Locate and identify every blood parasite.
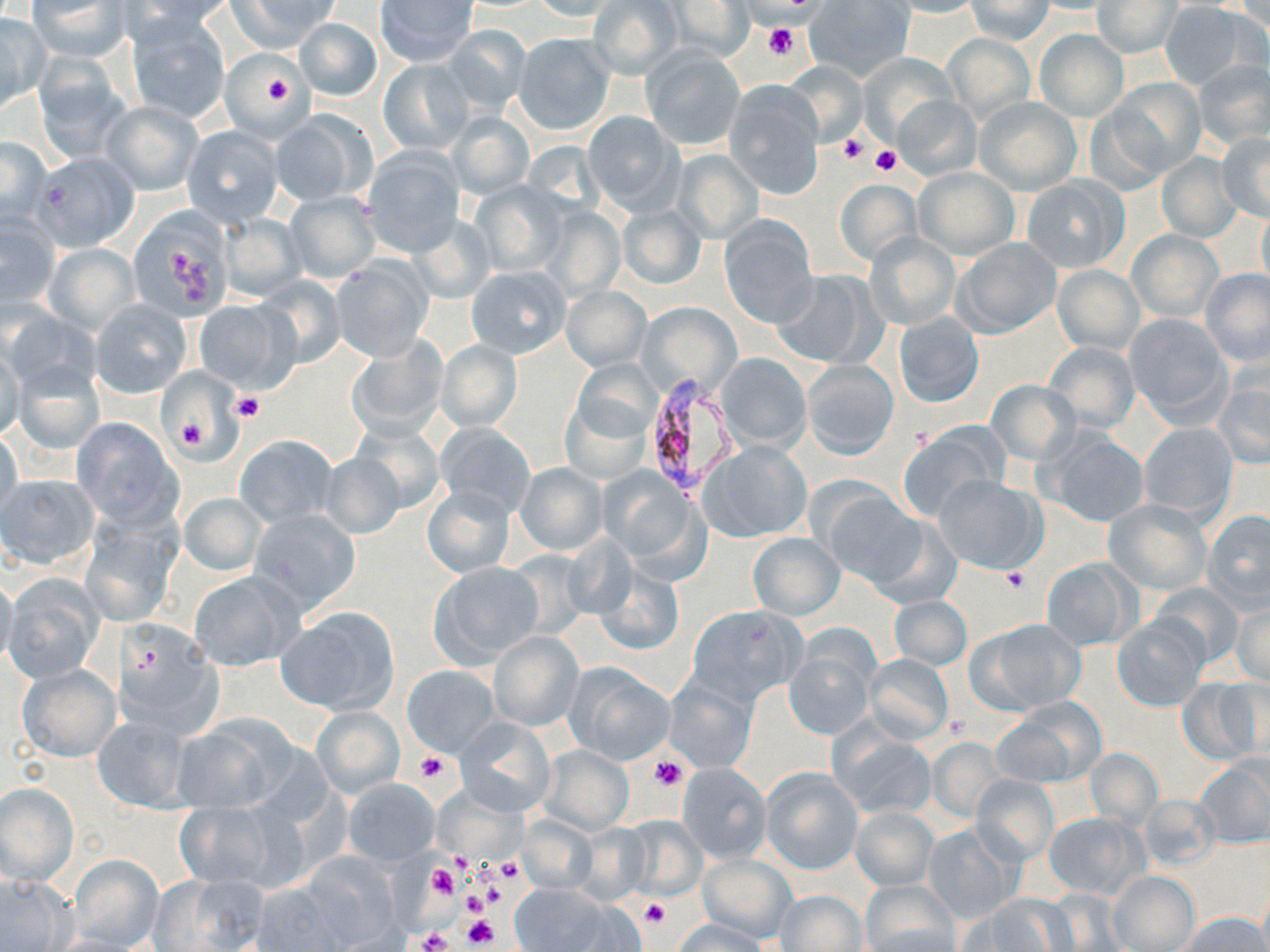
Approximate bounding boxes as (x1, y1, x2, y2) in pixels.
Plasmodium falciparum-infected red blood cells: (640, 375, 740, 498).
No Plasmodium ovale, Plasmodium malariae, Plasmodium vivax, Babesia divergens, or Trypanosoma brucei observed.

slide-level diagnosis = Plasmodium falciparum
preparation = thin blood film
platelet locations = approximate bounding boxes as (x1, y1, x2, y2) in pixels: (764, 24, 798, 58), (253, 66, 298, 112), (838, 131, 870, 163), (843, 138, 888, 170), (869, 147, 901, 176), (233, 393, 265, 421), (170, 408, 218, 458), (1002, 568, 1031, 592), (415, 751, 451, 784), (648, 755, 689, 792), (452, 852, 473, 877), (495, 857, 526, 884), (427, 864, 458, 899), (478, 879, 509, 909), (457, 890, 489, 919), (639, 899, 670, 929), (463, 914, 499, 948), (415, 927, 453, 952)
modality = light microscopy
image size = 1270×952 pixels
uninfected red blood cell locations = approximate bounding boxes as (x1, y1, x2, y2) in pixels: (27, 0, 131, 62), (124, 0, 236, 35), (376, 0, 479, 66), (659, 0, 759, 63), (803, 0, 916, 82), (882, 0, 984, 18), (228, 1, 337, 52), (526, 1, 625, 22), (588, 1, 684, 79), (964, 1, 1056, 43), (1094, 1, 1182, 58), (1158, 4, 1256, 89), (0, 13, 47, 111), (123, 14, 232, 124), (293, 17, 383, 101), (439, 24, 533, 115), (1034, 29, 1129, 122), (511, 33, 615, 135), (942, 34, 1035, 125), (639, 46, 747, 151), (221, 52, 309, 135), (856, 54, 959, 146), (378, 58, 472, 155), (1194, 59, 1270, 150), (33, 60, 131, 163), (781, 60, 867, 148), (1106, 78, 1207, 176), (722, 81, 826, 198), (893, 95, 983, 181), (973, 97, 1081, 195), (101, 101, 202, 195), (269, 111, 378, 207), (447, 111, 535, 199), (582, 111, 686, 216), (181, 126, 283, 226), (1215, 131, 1270, 224), (0, 135, 51, 229), (361, 149, 466, 257), (671, 149, 764, 243), (31, 151, 139, 251), (1155, 152, 1242, 243), (914, 166, 1019, 259), (1019, 175, 1128, 273), (832, 180, 924, 266), (470, 181, 572, 277), (284, 190, 381, 284), (1256, 203, 1270, 300), (614, 204, 707, 291), (539, 206, 625, 301), (124, 207, 234, 319), (218, 213, 305, 301), (407, 214, 497, 303), (718, 215, 819, 328), (1, 216, 62, 311), (1127, 229, 1225, 324), (864, 233, 960, 331), (952, 238, 1062, 339), (43, 243, 139, 334), (329, 255, 435, 361), (1052, 264, 1144, 354), (466, 265, 571, 359), (1200, 268, 1270, 368), (771, 269, 885, 371), (251, 275, 348, 368), (561, 286, 652, 371), (90, 300, 191, 397), (192, 300, 300, 393), (634, 302, 742, 402), (2, 306, 95, 396), (1123, 310, 1234, 427), (893, 311, 985, 409), (345, 336, 449, 438), (0, 337, 24, 445), (435, 340, 523, 432), (1042, 341, 1140, 433), (716, 352, 811, 452), (11, 357, 107, 456), (570, 359, 661, 445), (801, 360, 899, 460), (157, 369, 242, 460), (1212, 372, 1270, 471), (28, 378, 136, 495), (986, 380, 1079, 465), (560, 395, 653, 487), (70, 417, 180, 524), (347, 420, 444, 516), (434, 421, 536, 517), (897, 421, 1011, 523), (1137, 422, 1240, 524), (1034, 424, 1149, 528), (0, 426, 22, 525), (234, 434, 340, 529), (700, 440, 813, 544), (319, 454, 405, 536), (514, 463, 607, 555), (599, 467, 710, 580), (1, 474, 99, 570), (933, 474, 1047, 575), (817, 484, 922, 585), (422, 486, 515, 578), (178, 490, 268, 576), (1103, 499, 1212, 595), (248, 508, 363, 615), (1202, 510, 1270, 613), (81, 511, 182, 628), (862, 515, 961, 610), (747, 532, 846, 620), (1041, 558, 1137, 651), (427, 562, 545, 668), (594, 563, 684, 657), (0, 571, 18, 670), (188, 571, 303, 670), (4, 575, 103, 682), (1149, 582, 1243, 668), (888, 595, 973, 671), (1231, 601, 1270, 687), (687, 604, 806, 706), (274, 606, 401, 715), (1112, 615, 1209, 711), (969, 618, 1087, 715), (113, 619, 223, 738), (487, 630, 583, 732), (783, 642, 878, 741), (862, 654, 954, 744), (565, 662, 674, 765), (17, 663, 120, 762), (402, 666, 499, 757), (663, 672, 759, 771), (1180, 675, 1267, 764), (995, 697, 1106, 788), (312, 706, 404, 799), (93, 714, 194, 813), (168, 715, 296, 815), (453, 716, 557, 816), (831, 728, 938, 820), (927, 738, 1006, 821), (538, 745, 634, 834), (1085, 748, 1163, 828), (1196, 757, 1270, 849), (677, 763, 772, 863), (760, 766, 864, 875), (970, 774, 1058, 865), (341, 777, 441, 866), (0, 782, 77, 884), (1137, 793, 1222, 871), (174, 800, 284, 891), (849, 806, 937, 890), (1043, 812, 1146, 898), (518, 813, 600, 895), (619, 816, 709, 899), (572, 823, 652, 904), (922, 824, 1023, 925), (68, 853, 163, 951), (697, 854, 797, 944), (261, 857, 402, 952), (1109, 871, 1199, 951), (154, 873, 269, 952), (0, 875, 73, 950), (859, 881, 961, 951), (509, 883, 617, 951), (774, 889, 869, 952), (1042, 889, 1129, 950), (975, 895, 1075, 951), (1181, 913, 1266, 951), (674, 919, 770, 951)
stain = May-Grünwald-Giemsa
field of view = one of a larger specimen
magnification = 1000x